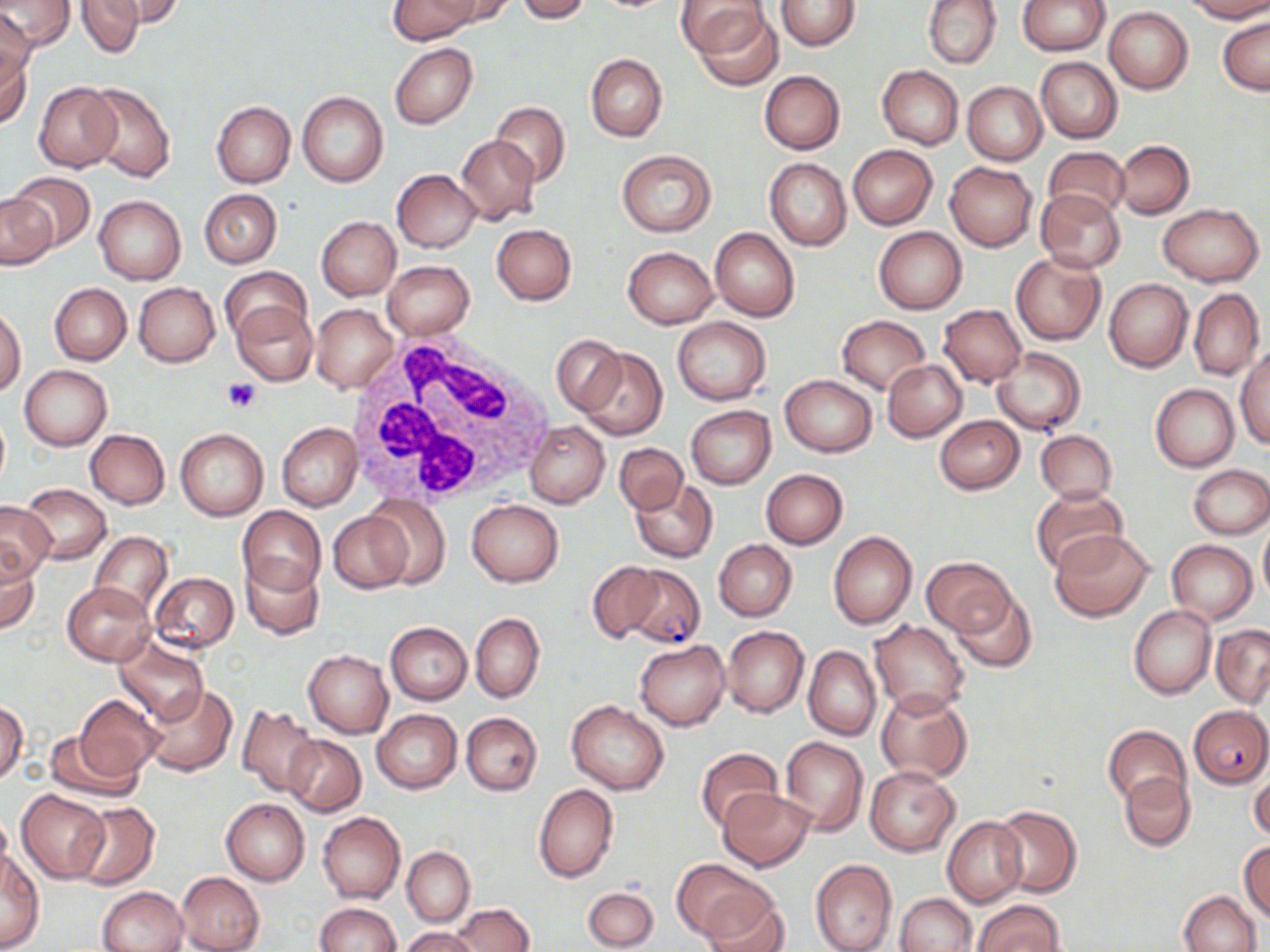

{
  "slide_level_diagnosis": "Plasmodium falciparum",
  "modality": "light microscopy",
  "plasmodium_falciparum_infected_red_blood_cell_locations": "approximate bounding boxes as (x1, y1, x2, y2) in pixels: (623, 565, 705, 648), (1188, 705, 1269, 788)",
  "white_blood_cell_locations": "approximate bounding boxes as (x1, y1, x2, y2) in pixels: (347, 332, 558, 509)",
  "uninfected_red_blood_cell_locations": "approximate bounding boxes as (x1, y1, x2, y2) in pixels: (1, 0, 72, 52), (97, 0, 184, 29), (389, 0, 479, 44), (432, 0, 517, 29), (516, 0, 591, 22), (775, 0, 860, 51), (923, 0, 1001, 69), (928, 0, 1009, 141), (1016, 0, 1110, 56), (1183, 0, 1270, 21), (74, 1, 150, 57), (678, 2, 770, 58), (1104, 7, 1193, 94), (0, 8, 37, 94), (693, 8, 784, 90), (1218, 16, 1269, 95), (0, 43, 33, 132), (389, 43, 477, 129), (586, 53, 668, 142), (1035, 57, 1122, 143), (877, 66, 963, 149), (759, 71, 845, 155), (963, 71, 1122, 152), (962, 81, 1047, 165), (33, 82, 122, 172), (83, 83, 177, 183), (297, 90, 388, 187), (212, 101, 295, 187), (491, 101, 570, 187), (456, 135, 540, 223), (1113, 140, 1194, 219), (848, 145, 938, 229), (1042, 146, 1130, 220), (617, 149, 716, 236), (764, 158, 851, 250), (944, 162, 1038, 252), (391, 169, 481, 252), (7, 171, 94, 251), (199, 188, 281, 267), (1036, 190, 1125, 273), (1, 195, 57, 269), (93, 195, 186, 285), (1158, 203, 1263, 286), (316, 217, 401, 300), (492, 224, 577, 305), (874, 226, 966, 313), (710, 228, 800, 321), (623, 245, 717, 327), (1010, 251, 1105, 345), (382, 260, 475, 340), (220, 266, 310, 345), (1103, 277, 1193, 372), (50, 282, 132, 365), (132, 282, 220, 366), (1188, 289, 1265, 380), (232, 300, 318, 386), (311, 304, 398, 393), (938, 304, 1027, 388), (0, 307, 26, 396), (836, 314, 931, 393), (672, 316, 771, 405), (552, 335, 626, 415), (577, 346, 667, 439), (1236, 346, 1270, 448), (991, 347, 1086, 436), (882, 360, 967, 441), (20, 365, 112, 450), (779, 374, 877, 457), (1151, 384, 1238, 471), (686, 405, 775, 489), (935, 415, 1024, 494), (525, 421, 609, 507), (277, 422, 362, 510), (176, 428, 269, 520), (85, 430, 170, 509), (1035, 430, 1117, 504), (614, 442, 687, 515), (1186, 464, 1269, 540), (761, 468, 848, 548), (630, 477, 717, 562), (21, 484, 111, 565), (1030, 487, 1127, 575), (363, 498, 451, 587), (466, 499, 564, 587), (0, 500, 55, 582), (238, 506, 326, 595), (327, 512, 414, 594), (1258, 522, 1270, 602), (1049, 528, 1156, 621), (828, 530, 918, 629), (90, 531, 172, 616), (714, 539, 797, 620), (1166, 539, 1257, 624), (0, 553, 42, 634), (922, 556, 1016, 635), (242, 557, 323, 640), (587, 561, 665, 643), (149, 572, 238, 654), (62, 581, 155, 665), (948, 590, 1037, 673), (1130, 606, 1214, 698), (470, 613, 544, 703), (870, 620, 969, 717), (385, 622, 472, 704), (722, 624, 808, 717), (1211, 625, 1270, 707), (115, 638, 207, 724), (635, 640, 730, 730), (804, 646, 880, 741), (303, 650, 392, 738), (141, 684, 237, 776), (877, 688, 973, 785), (74, 694, 162, 781), (567, 700, 669, 794), (1, 701, 27, 784), (237, 704, 320, 798), (371, 709, 461, 793), (461, 712, 543, 796), (1103, 725, 1189, 808), (43, 729, 142, 804), (282, 735, 366, 815), (779, 737, 867, 837), (695, 747, 781, 833), (864, 765, 961, 857), (1248, 767, 1270, 844), (1119, 771, 1195, 852), (533, 783, 618, 883), (718, 788, 814, 871), (16, 790, 110, 883), (221, 798, 309, 885), (72, 801, 159, 890), (991, 805, 1081, 897), (0, 808, 13, 884), (317, 812, 405, 903), (942, 815, 1029, 907), (1239, 842, 1270, 924), (402, 846, 474, 925), (0, 851, 43, 950), (672, 859, 772, 942), (811, 859, 896, 952), (177, 872, 265, 952), (98, 886, 188, 952), (583, 887, 658, 950), (1180, 889, 1262, 952), (700, 890, 791, 952), (896, 892, 976, 952), (972, 899, 1063, 951), (452, 902, 535, 952), (313, 903, 402, 952), (399, 927, 480, 952)",
  "field_of_view": "single",
  "platelet_locations": "approximate bounding boxes as (x1, y1, x2, y2) in pixels: (222, 379, 260, 413)",
  "image_size": "1270×952 pixels",
  "preparation": "thin blood film",
  "magnification": "1000x",
  "stain": "May-Grünwald-Giemsa"
}